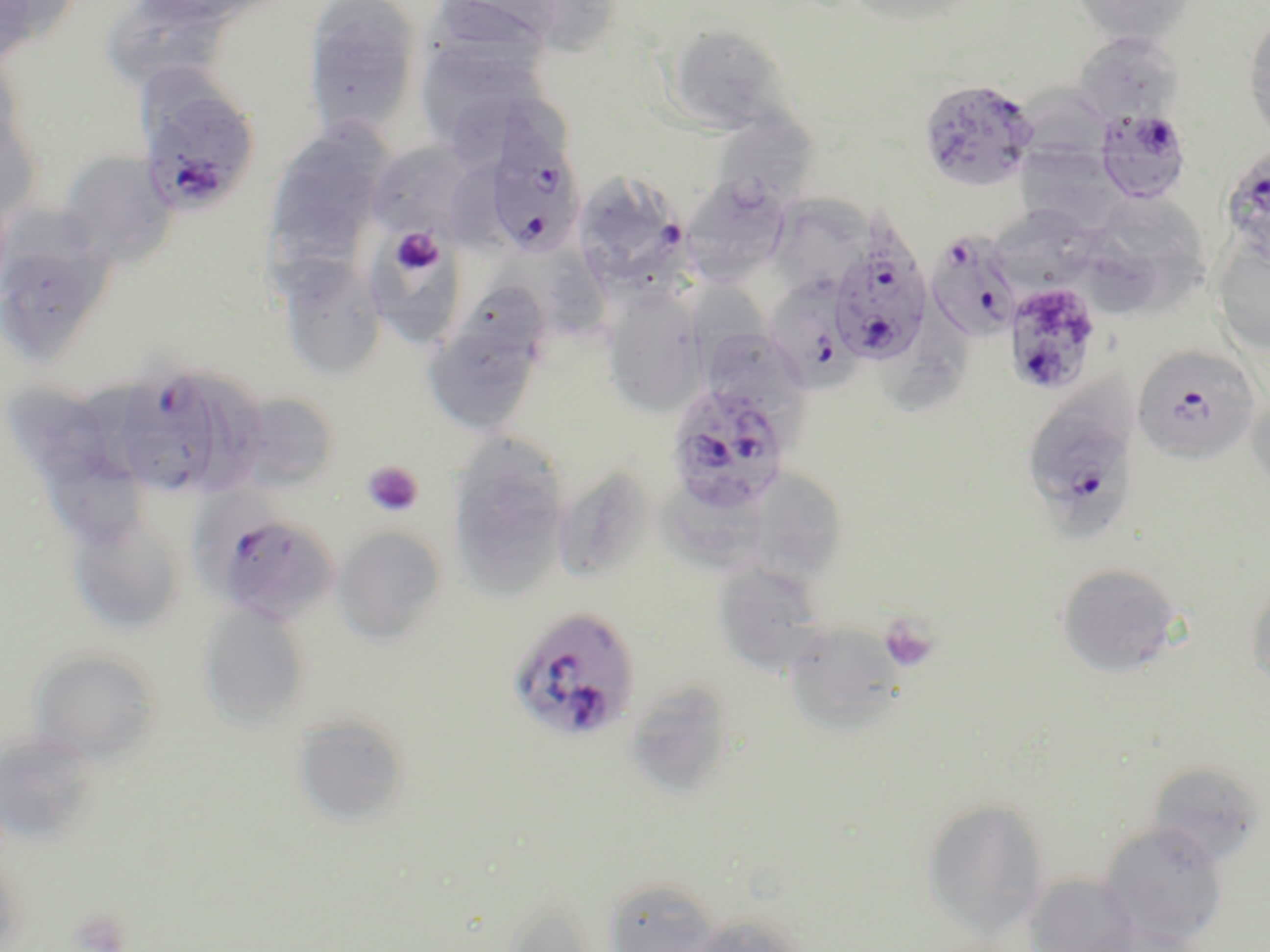
Approximate bounding boxes as [x1, y1, x2, y2] in pixels. Platelet locations: [389, 227, 443, 277], [362, 461, 424, 517], [879, 614, 940, 673], [67, 907, 133, 952]. Plasmodium falciparum-infected red blood cell locations: [918, 77, 1039, 192], [135, 79, 261, 220], [1093, 108, 1191, 204], [479, 126, 584, 261], [1220, 146, 1270, 266], [583, 169, 694, 292], [931, 229, 1022, 340], [828, 234, 933, 367], [771, 274, 865, 397], [1002, 281, 1102, 396], [1131, 343, 1261, 464], [109, 363, 223, 500], [666, 382, 792, 514], [1021, 386, 1141, 537], [203, 508, 340, 624], [507, 605, 640, 744]. Uninfected red blood cell locations: [1, 0, 71, 60], [129, 0, 287, 30], [303, 0, 422, 142], [427, 0, 569, 60], [842, 0, 981, 27], [1072, 0, 1200, 46], [101, 1, 230, 97], [1244, 14, 1270, 145], [666, 25, 791, 134], [1072, 31, 1184, 127], [414, 37, 546, 155], [0, 83, 41, 226], [721, 108, 827, 205], [264, 121, 396, 265], [1016, 142, 1124, 234], [366, 144, 475, 241], [57, 152, 177, 271], [682, 177, 790, 285], [1082, 191, 1211, 311], [765, 194, 881, 289], [993, 211, 1114, 288], [0, 215, 118, 365], [1212, 238, 1270, 355], [373, 248, 466, 353], [493, 251, 610, 343], [276, 256, 387, 383], [698, 274, 778, 383], [602, 288, 708, 418], [422, 308, 546, 436], [709, 330, 813, 444], [198, 372, 263, 505], [1247, 389, 1270, 502], [7, 391, 108, 490], [229, 391, 338, 494], [446, 435, 571, 599], [38, 441, 152, 556], [552, 464, 656, 586], [753, 467, 843, 599], [662, 480, 768, 573], [66, 513, 187, 637], [333, 526, 448, 645], [712, 561, 829, 676], [1055, 561, 1185, 680], [1245, 576, 1270, 694], [197, 600, 313, 732], [789, 623, 905, 737], [27, 645, 163, 764], [621, 678, 739, 800], [291, 712, 413, 828], [1, 729, 102, 848], [1147, 760, 1265, 868], [920, 795, 1052, 940], [1097, 821, 1229, 948], [0, 853, 29, 951], [1023, 872, 1143, 952], [602, 874, 722, 952], [498, 899, 603, 951], [686, 910, 811, 952]. Slide-level diagnosis: Plasmodium falciparum. Optical microscopy. One field of a larger specimen. Captured at 1000x magnification. Thin blood smear. Image is 1270×952 pixels. May-Grünwald-Giemsa-stained preparation.